Locate and identify every blood parasite.
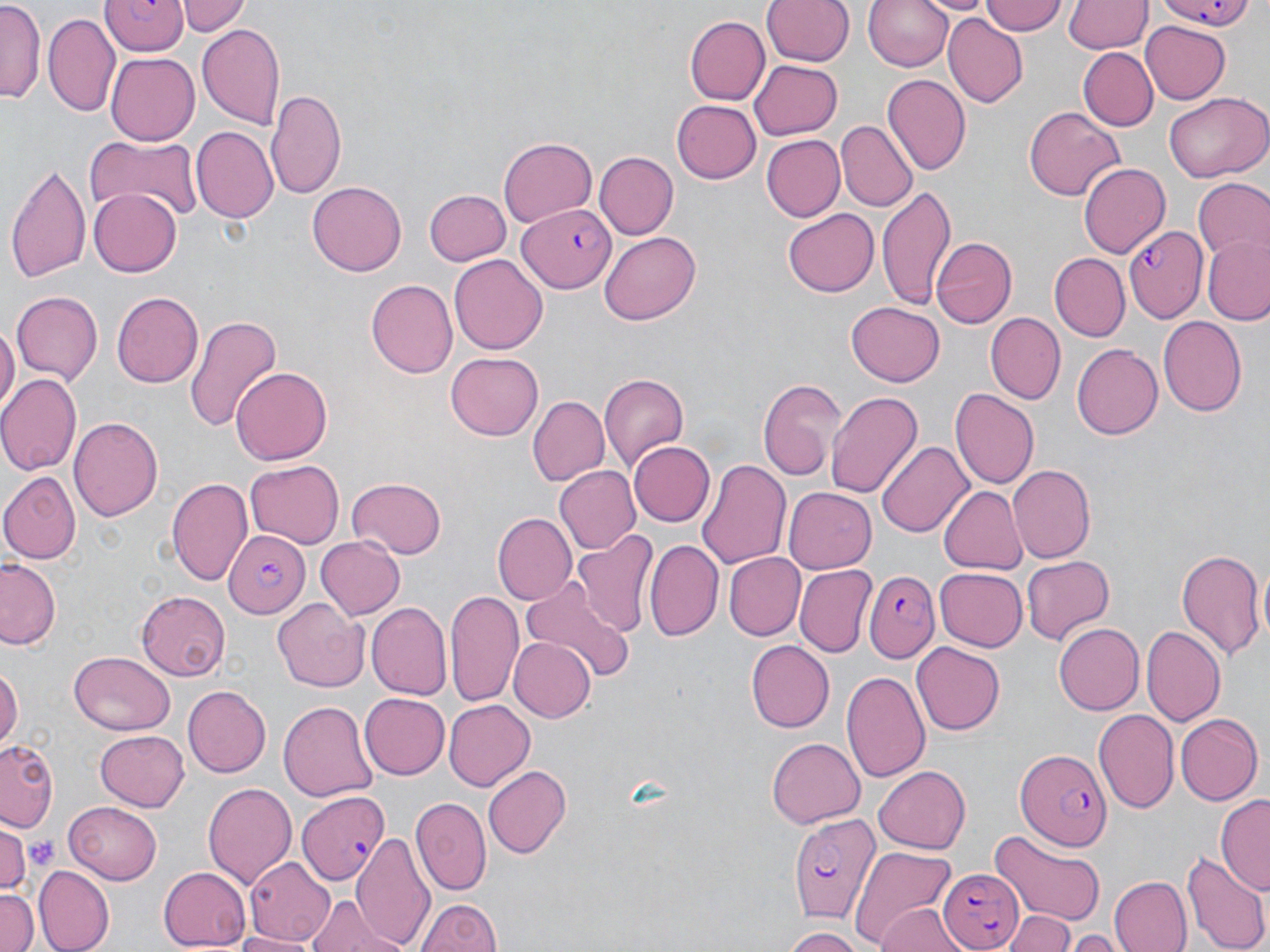
Approximate bounding boxes as (x1, y1, x2, y2) in pixels.
Plasmodium falciparum-infected red blood cells: (102, 0, 191, 57), (1157, 1, 1259, 34), (517, 202, 616, 294), (1126, 224, 1209, 318), (223, 527, 307, 617), (864, 569, 941, 661), (1013, 744, 1112, 850), (296, 792, 389, 882), (786, 810, 879, 922), (937, 866, 1021, 950).
No Plasmodium ovale, Plasmodium malariae, Plasmodium vivax, Babesia divergens, or Trypanosoma brucei observed.

Platelet locations: (26, 834, 57, 871). Uninfected red blood cell locations: (181, 0, 248, 37), (762, 0, 853, 66), (864, 0, 956, 72), (925, 0, 991, 18), (981, 0, 1067, 37), (1063, 0, 1149, 55), (1, 4, 46, 104), (44, 11, 119, 115), (683, 15, 770, 106), (944, 16, 1027, 104), (1142, 22, 1231, 104), (198, 23, 285, 130), (1077, 46, 1157, 131), (106, 52, 199, 144), (751, 60, 843, 140), (882, 75, 971, 176), (267, 89, 348, 200), (1163, 94, 1267, 182), (672, 100, 761, 183), (1022, 106, 1124, 202), (837, 122, 917, 212), (190, 126, 277, 223), (760, 134, 844, 222), (89, 135, 204, 225), (497, 137, 597, 231), (596, 153, 677, 239), (6, 161, 90, 284), (1079, 163, 1168, 260), (1192, 178, 1270, 261), (307, 180, 408, 277), (88, 186, 183, 278), (876, 186, 956, 309), (424, 188, 512, 265), (782, 210, 878, 298), (598, 231, 702, 326), (932, 234, 1018, 329), (1202, 237, 1270, 325), (1047, 252, 1130, 341), (449, 254, 548, 355), (367, 279, 460, 378), (9, 291, 104, 385), (111, 291, 204, 388), (846, 300, 944, 386), (984, 312, 1066, 405), (1157, 313, 1246, 413), (183, 314, 280, 431), (0, 325, 17, 416), (1071, 343, 1163, 440), (446, 353, 543, 440), (231, 365, 330, 464), (0, 372, 81, 476), (601, 372, 689, 470), (756, 377, 845, 482), (949, 389, 1037, 491), (827, 390, 924, 497), (529, 397, 608, 486), (71, 415, 163, 524), (629, 439, 716, 527), (876, 439, 973, 537), (697, 456, 791, 571), (244, 461, 342, 549), (1009, 464, 1096, 562), (553, 465, 639, 554), (0, 472, 79, 564), (166, 475, 254, 586), (346, 478, 448, 559), (938, 483, 1028, 574), (784, 487, 876, 575), (492, 512, 575, 604), (572, 530, 659, 639), (314, 535, 405, 620), (645, 539, 723, 642), (1175, 548, 1265, 664), (724, 552, 805, 641), (1019, 555, 1117, 646), (1, 558, 61, 649), (795, 566, 876, 657), (934, 567, 1027, 650), (520, 583, 635, 681), (446, 588, 527, 709), (137, 590, 231, 679), (272, 598, 369, 691), (367, 602, 451, 699), (1054, 623, 1145, 714), (1141, 624, 1226, 728), (508, 637, 595, 722), (744, 640, 834, 732), (912, 642, 1004, 737), (67, 652, 175, 735), (0, 665, 21, 754), (841, 671, 929, 785), (183, 686, 272, 776), (359, 693, 449, 779), (278, 698, 377, 802), (442, 701, 533, 790), (1092, 709, 1178, 813), (1174, 714, 1259, 806), (96, 729, 189, 811), (767, 736, 865, 828), (0, 738, 61, 833), (484, 764, 572, 858), (873, 766, 972, 853), (202, 781, 297, 891), (1216, 794, 1270, 894), (411, 797, 492, 895), (63, 803, 166, 885), (0, 825, 34, 895), (352, 830, 433, 948), (990, 831, 1106, 922), (850, 846, 956, 950), (1184, 849, 1270, 952), (245, 857, 336, 946), (159, 865, 252, 950), (34, 866, 113, 950), (1108, 876, 1192, 952), (0, 887, 38, 952), (307, 896, 404, 950), (415, 897, 502, 952), (873, 905, 972, 952), (1003, 908, 1079, 952), (783, 927, 875, 950), (231, 930, 310, 952), (1067, 934, 1121, 950). Slide-level diagnosis: Plasmodium falciparum. One field of a larger specimen. Image is 1270×952 pixels. 1000x magnification. Light microscopy. May-Grünwald-Giemsa stain. Thin blood film.